Locate every Plasmodium parasite.
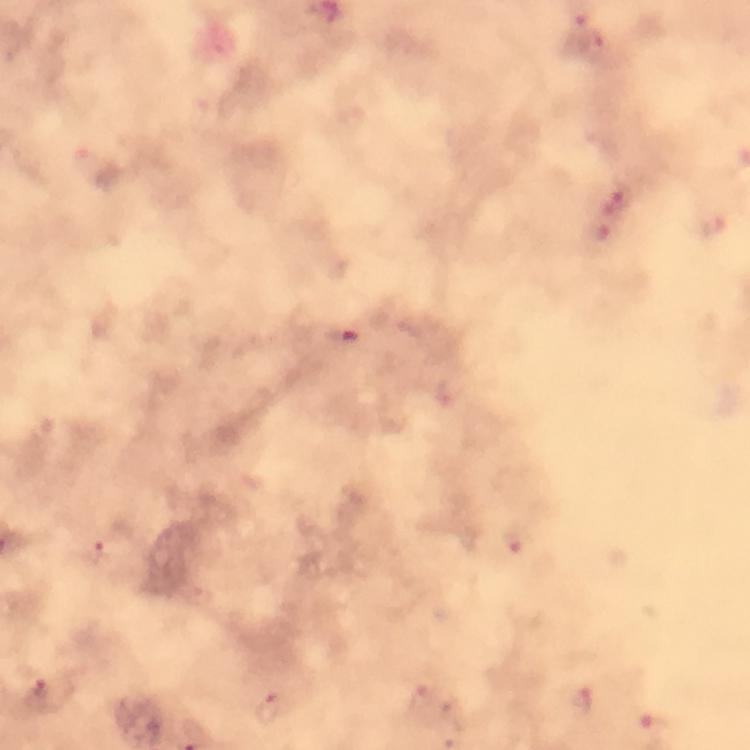

Approximate object centers, in pixels from the top-left corner.
Plasmodium parasites: (x=594, y=48), (x=614, y=197), (x=714, y=225), (x=605, y=233), (x=344, y=336), (x=513, y=544), (x=94, y=552), (x=38, y=690), (x=420, y=699), (x=584, y=699), (x=271, y=708), (x=659, y=723).

image_size: 750×750 pixels
cropped_from: one field of view
magnification: 100x
capture: smartphone photograph through a microscope
immersion_oil: applied
preparation: thick blood film
stain: Giemsa
context: from a diagnostic examination for malaria